Classify this cell by malaria status.
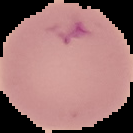
Uninfected.

Summary:
  - Image type: segmented cell region on a black background
  - Preparation: thin blood smear
  - Image size: 133×133 pixels